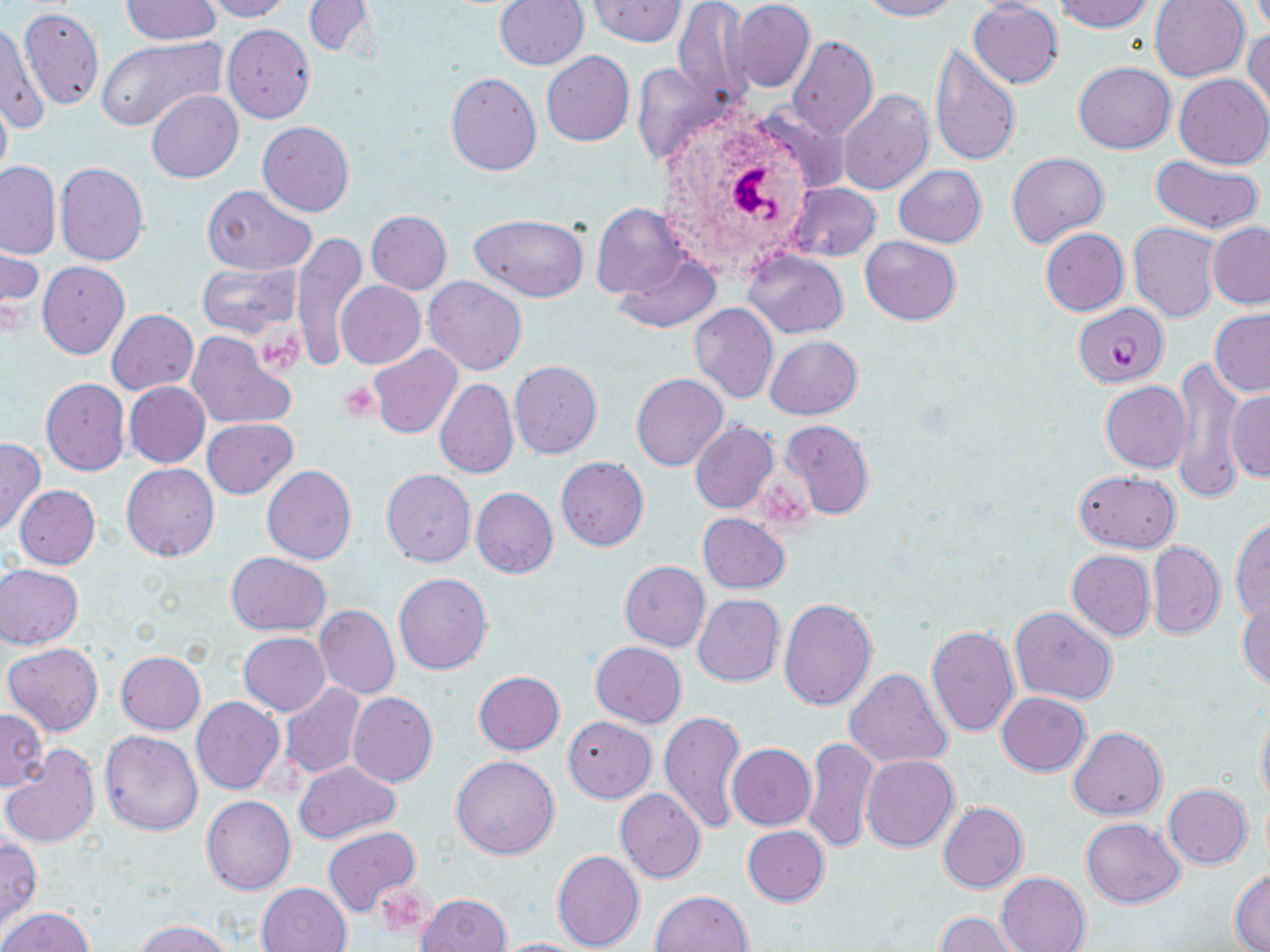
{
  "slide_level_diagnosis": "Plasmodium falciparum",
  "uninfected_red_blood_cell_locations": "approximate bounding boxes as (x1, y1, x2, y2) in pixels: (119, 0, 221, 44), (199, 0, 294, 21), (496, 0, 588, 70), (588, 0, 684, 46), (672, 0, 749, 111), (858, 0, 963, 21), (1057, 0, 1154, 33), (1150, 0, 1250, 82), (304, 1, 373, 57), (733, 1, 814, 92), (969, 2, 1064, 87), (19, 7, 105, 111), (1, 17, 46, 135), (223, 24, 316, 124), (1244, 25, 1270, 119), (97, 34, 225, 130), (788, 35, 877, 139), (928, 45, 1021, 167), (542, 51, 634, 146), (631, 61, 724, 169), (1074, 61, 1175, 154), (445, 73, 542, 175), (1173, 74, 1269, 169), (838, 89, 933, 194), (147, 90, 242, 183), (0, 92, 11, 191), (257, 122, 354, 216), (1007, 151, 1108, 249), (1150, 155, 1266, 234), (0, 160, 61, 258), (55, 162, 149, 266), (894, 165, 986, 247), (786, 182, 880, 261), (202, 186, 318, 275), (592, 204, 688, 298), (366, 210, 452, 294), (470, 213, 589, 301), (1208, 222, 1270, 307), (1129, 223, 1220, 322), (1040, 228, 1129, 316), (291, 234, 369, 369), (861, 236, 961, 325), (0, 243, 42, 331), (744, 249, 848, 339), (615, 253, 721, 333), (198, 260, 300, 340), (37, 262, 130, 359), (424, 277, 528, 375), (337, 281, 426, 369), (689, 303, 778, 403), (1209, 309, 1270, 396), (107, 310, 199, 395), (185, 332, 295, 430), (764, 336, 863, 419), (369, 345, 462, 439), (1171, 360, 1245, 501), (509, 361, 602, 458), (631, 373, 727, 471), (40, 377, 129, 476), (434, 379, 518, 479), (124, 381, 210, 467), (1101, 381, 1192, 472), (1227, 387, 1268, 483), (203, 418, 297, 498), (780, 419, 875, 519), (690, 420, 778, 514), (0, 439, 45, 535), (555, 457, 648, 550), (122, 462, 219, 561), (262, 464, 358, 564), (382, 469, 476, 567), (1074, 470, 1181, 552), (14, 484, 100, 569), (471, 487, 558, 578), (697, 513, 790, 594), (1231, 516, 1270, 623), (1148, 541, 1226, 639), (1067, 550, 1155, 640), (226, 552, 331, 637), (619, 560, 710, 650), (0, 565, 84, 649), (393, 573, 492, 674), (692, 594, 784, 685), (1237, 596, 1270, 691), (779, 597, 877, 712), (315, 606, 399, 700), (1010, 607, 1118, 704), (925, 625, 1019, 737), (238, 632, 330, 715), (591, 641, 686, 727), (3, 642, 104, 736), (116, 651, 206, 734), (845, 668, 951, 769), (474, 671, 565, 755), (279, 684, 365, 780), (348, 692, 437, 787), (997, 692, 1090, 775), (192, 696, 285, 794), (1256, 704, 1270, 810), (0, 709, 47, 790), (659, 710, 747, 833), (563, 717, 656, 802), (1068, 727, 1167, 820), (100, 731, 203, 835), (803, 736, 879, 853), (0, 739, 201, 840), (727, 743, 816, 830), (2, 747, 100, 848), (450, 755, 560, 859), (860, 755, 959, 852), (293, 760, 401, 844), (1163, 784, 1252, 868), (615, 788, 706, 883), (202, 796, 297, 894), (938, 802, 1029, 893), (1080, 817, 1185, 908), (741, 825, 829, 907), (323, 826, 421, 919), (0, 837, 42, 932), (553, 850, 646, 951), (1230, 869, 1270, 951), (996, 872, 1091, 951), (257, 882, 352, 952), (649, 890, 755, 952), (417, 892, 511, 952), (2, 906, 93, 952), (936, 913, 1022, 952), (136, 919, 234, 952), (490, 938, 590, 952)",
  "magnification": "1000x",
  "preparation": "thin blood smear",
  "platelet_locations": "approximate bounding boxes as (x1, y1, x2, y2) in pixels: (255, 330, 307, 376), (338, 382, 382, 421), (373, 885, 428, 934)",
  "field_of_view": "one of a larger specimen",
  "plasmodium_falciparum_infected_red_blood_cell_locations": "approximate bounding boxes as (x1, y1, x2, y2) in pixels: (1074, 300, 1167, 387)",
  "stain": "May-Grünwald-Giemsa",
  "image_size": "1270×952 pixels",
  "modality": "light microscopy"
}